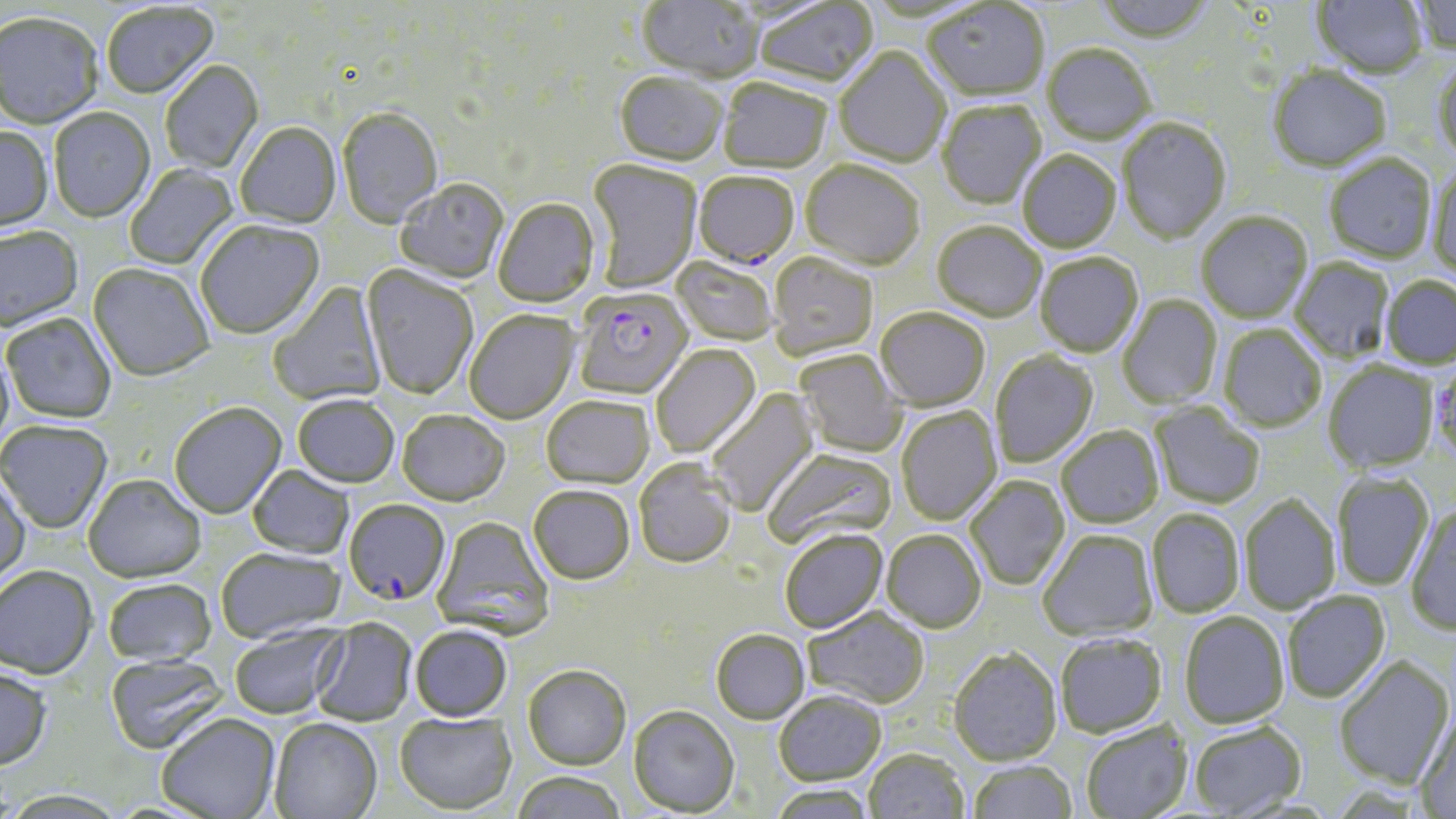

slide-level diagnosis = Plasmodium falciparum
modality = optical microscopy
Plasmodium falciparum-infected red blood cell locations = approximate bounding boxes as named x1/y1/x2/y2 corners in pixels: (x1=694, y1=174, x2=799, y2=271), (x1=573, y1=289, x2=693, y2=401), (x1=344, y1=500, x2=450, y2=606)
uninfected red blood cell locations = approximate bounding boxes as named x1/y1/x2/y2 corners in pixels: (x1=636, y1=0, x2=764, y2=85), (x1=1092, y1=0, x2=1215, y2=47), (x1=1312, y1=0, x2=1428, y2=78), (x1=1409, y1=0, x2=1456, y2=54), (x1=754, y1=1, x2=879, y2=90), (x1=923, y1=2, x2=1049, y2=103), (x1=101, y1=3, x2=218, y2=102), (x1=0, y1=14, x2=104, y2=131), (x1=1042, y1=46, x2=1155, y2=146), (x1=834, y1=48, x2=950, y2=169), (x1=1432, y1=56, x2=1456, y2=165), (x1=160, y1=62, x2=264, y2=174), (x1=1267, y1=66, x2=1392, y2=173), (x1=614, y1=74, x2=727, y2=169), (x1=718, y1=80, x2=831, y2=175), (x1=937, y1=102, x2=1047, y2=210), (x1=49, y1=109, x2=155, y2=224), (x1=337, y1=109, x2=443, y2=230), (x1=1117, y1=118, x2=1231, y2=245), (x1=236, y1=124, x2=342, y2=230), (x1=0, y1=128, x2=53, y2=234), (x1=1018, y1=152, x2=1121, y2=254), (x1=1324, y1=155, x2=1436, y2=263), (x1=586, y1=160, x2=702, y2=294), (x1=125, y1=163, x2=238, y2=271), (x1=801, y1=163, x2=925, y2=273), (x1=1427, y1=166, x2=1456, y2=279), (x1=395, y1=180, x2=509, y2=284), (x1=494, y1=200, x2=600, y2=309), (x1=1196, y1=212, x2=1313, y2=323), (x1=195, y1=221, x2=325, y2=341), (x1=932, y1=223, x2=1045, y2=324), (x1=0, y1=228, x2=84, y2=334), (x1=768, y1=254, x2=877, y2=361), (x1=1035, y1=254, x2=1144, y2=358), (x1=671, y1=258, x2=778, y2=346), (x1=1291, y1=259, x2=1394, y2=363), (x1=88, y1=265, x2=214, y2=383), (x1=360, y1=265, x2=478, y2=400), (x1=1381, y1=276, x2=1456, y2=369), (x1=268, y1=283, x2=387, y2=405), (x1=1117, y1=296, x2=1222, y2=408), (x1=875, y1=309, x2=990, y2=412), (x1=464, y1=311, x2=579, y2=426), (x1=2, y1=314, x2=116, y2=424), (x1=1218, y1=325, x2=1327, y2=432), (x1=650, y1=345, x2=761, y2=459), (x1=0, y1=347, x2=14, y2=453), (x1=794, y1=350, x2=906, y2=458), (x1=990, y1=351, x2=1099, y2=468), (x1=1430, y1=360, x2=1455, y2=463), (x1=1323, y1=362, x2=1439, y2=474), (x1=706, y1=388, x2=821, y2=517), (x1=292, y1=397, x2=399, y2=489), (x1=541, y1=398, x2=653, y2=490), (x1=1150, y1=402, x2=1265, y2=509), (x1=169, y1=404, x2=287, y2=520), (x1=896, y1=408, x2=1002, y2=526), (x1=397, y1=412, x2=510, y2=508), (x1=0, y1=421, x2=112, y2=534), (x1=1057, y1=426, x2=1164, y2=528), (x1=763, y1=449, x2=897, y2=550), (x1=634, y1=459, x2=737, y2=569), (x1=247, y1=467, x2=355, y2=560), (x1=1331, y1=472, x2=1434, y2=591), (x1=0, y1=476, x2=30, y2=590), (x1=83, y1=476, x2=206, y2=583), (x1=965, y1=477, x2=1069, y2=590), (x1=528, y1=487, x2=635, y2=586), (x1=1239, y1=493, x2=1341, y2=615), (x1=1406, y1=503, x2=1456, y2=636), (x1=1147, y1=509, x2=1245, y2=618), (x1=432, y1=517, x2=554, y2=640), (x1=780, y1=530, x2=888, y2=634), (x1=1038, y1=530, x2=1158, y2=641), (x1=882, y1=531, x2=985, y2=634), (x1=216, y1=548, x2=346, y2=643), (x1=0, y1=566, x2=98, y2=679), (x1=103, y1=578, x2=216, y2=667), (x1=1282, y1=591, x2=1390, y2=703), (x1=803, y1=608, x2=929, y2=710), (x1=1179, y1=611, x2=1290, y2=729), (x1=311, y1=619, x2=416, y2=726), (x1=229, y1=623, x2=347, y2=719), (x1=410, y1=626, x2=512, y2=722), (x1=710, y1=629, x2=810, y2=724), (x1=1055, y1=635, x2=1167, y2=737), (x1=948, y1=648, x2=1062, y2=767), (x1=106, y1=654, x2=229, y2=754), (x1=1333, y1=655, x2=1455, y2=789), (x1=523, y1=664, x2=631, y2=769), (x1=0, y1=665, x2=52, y2=771), (x1=773, y1=691, x2=886, y2=785), (x1=628, y1=705, x2=739, y2=816), (x1=157, y1=712, x2=281, y2=818), (x1=395, y1=713, x2=515, y2=814), (x1=1415, y1=713, x2=1456, y2=818), (x1=269, y1=718, x2=383, y2=818), (x1=1189, y1=721, x2=1306, y2=817), (x1=1081, y1=722, x2=1192, y2=819), (x1=863, y1=749, x2=968, y2=819), (x1=966, y1=760, x2=1078, y2=819), (x1=511, y1=771, x2=627, y2=819), (x1=767, y1=784, x2=878, y2=819)
magnification = 1000x
preparation = thin blood film
stain = May-Grünwald-Giemsa
image size = 1456×819 pixels
field of view = one of a larger specimen